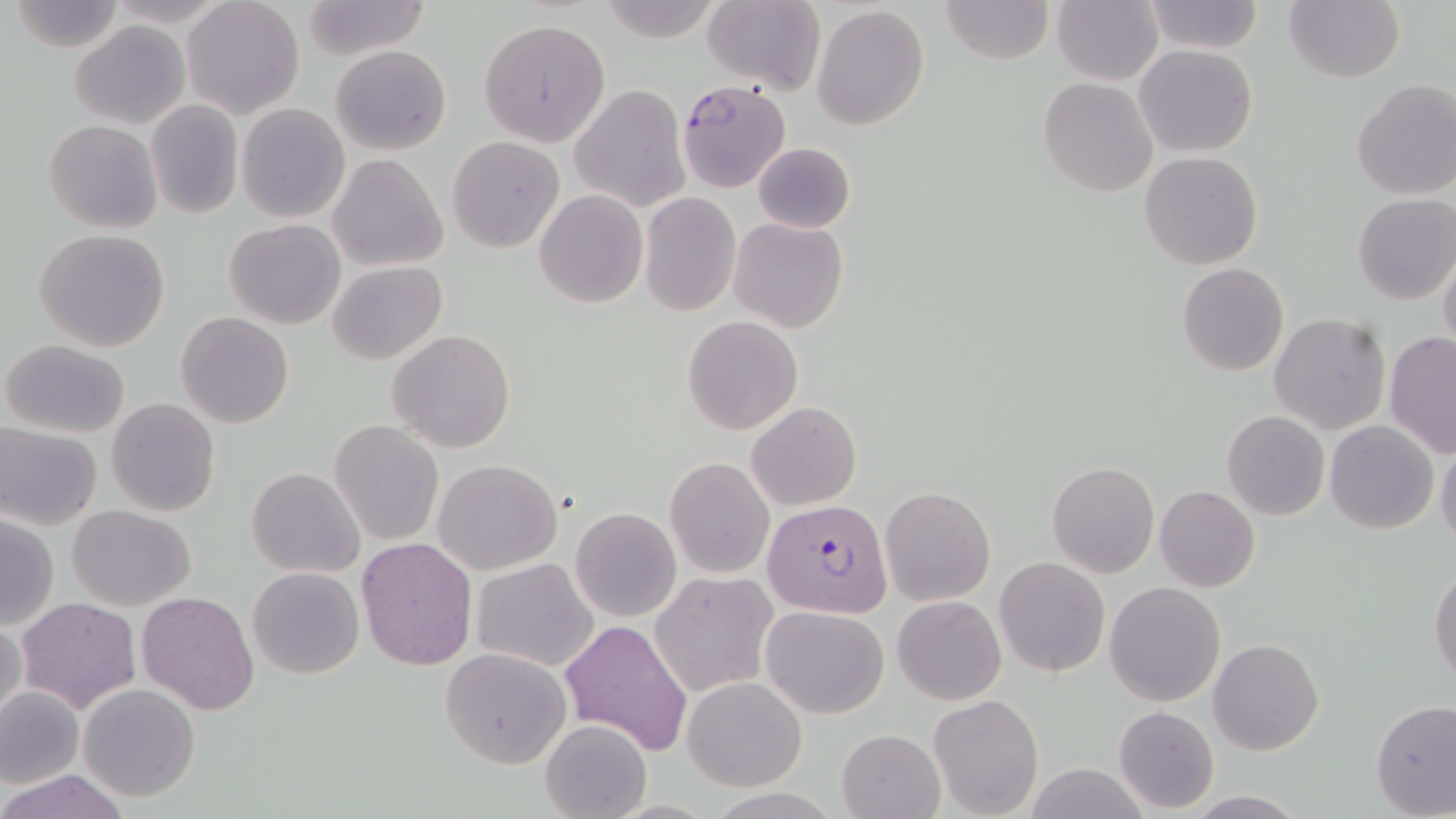

slide-level diagnosis = Plasmodium falciparum
modality = light microscopy
field of view = single
uninfected red blood cell locations = approximate bounding boxes as (x1, y1, x2, y2) in pixels: (301, 0, 434, 60), (596, 0, 727, 44), (939, 0, 1053, 65), (1052, 0, 1162, 85), (1284, 0, 1403, 82), (8, 1, 124, 51), (181, 1, 306, 118), (1142, 1, 1264, 53), (700, 2, 824, 93), (812, 3, 929, 131), (478, 17, 612, 147), (70, 21, 190, 128), (330, 44, 452, 154), (1134, 44, 1258, 158), (1039, 77, 1159, 198), (1350, 79, 1456, 200), (570, 84, 690, 211), (145, 101, 243, 218), (237, 103, 349, 223), (44, 120, 161, 235), (447, 135, 565, 253), (752, 143, 855, 233), (1139, 152, 1263, 270), (329, 155, 447, 271), (534, 189, 648, 308), (639, 191, 742, 317), (1352, 193, 1456, 304), (729, 217, 848, 332), (223, 219, 345, 329), (33, 229, 172, 352), (1438, 248, 1456, 357), (327, 261, 446, 364), (1177, 263, 1289, 377), (175, 312, 293, 428), (1269, 313, 1390, 434), (683, 315, 802, 435), (387, 329, 515, 453), (1383, 333, 1456, 457), (1, 339, 129, 437), (106, 397, 222, 517), (746, 401, 861, 512), (1222, 411, 1330, 520), (329, 420, 443, 546), (1325, 420, 1439, 535), (0, 423, 101, 530), (1436, 444, 1456, 551), (665, 456, 775, 578), (434, 458, 562, 574), (1047, 462, 1160, 578), (247, 467, 365, 578), (1154, 485, 1259, 592), (880, 486, 995, 605), (68, 505, 195, 610), (571, 507, 680, 622), (1, 515, 58, 631), (356, 537, 478, 671), (994, 556, 1109, 677), (471, 558, 599, 674), (1429, 561, 1456, 686), (248, 566, 363, 679), (651, 573, 777, 697), (1104, 582, 1226, 706), (136, 590, 258, 715), (892, 594, 1006, 705), (16, 597, 142, 715), (761, 605, 889, 718), (0, 617, 26, 728), (561, 618, 691, 756), (1208, 636, 1325, 756), (440, 648, 570, 769), (682, 677, 805, 790), (78, 684, 200, 802), (0, 686, 82, 789), (927, 694, 1044, 818), (1370, 701, 1456, 817), (1113, 704, 1219, 813), (540, 718, 650, 819), (836, 728, 944, 819), (1021, 765, 1148, 819), (2, 769, 129, 819), (1183, 791, 1311, 818)
image size = 1456×819 pixels
stain = May-Grünwald-Giemsa
magnification = 1000x
Plasmodium falciparum-infected red blood cell locations = approximate bounding boxes as (x1, y1, x2, y2) in pixels: (676, 81, 791, 192), (763, 498, 893, 618)
preparation = thin blood smear